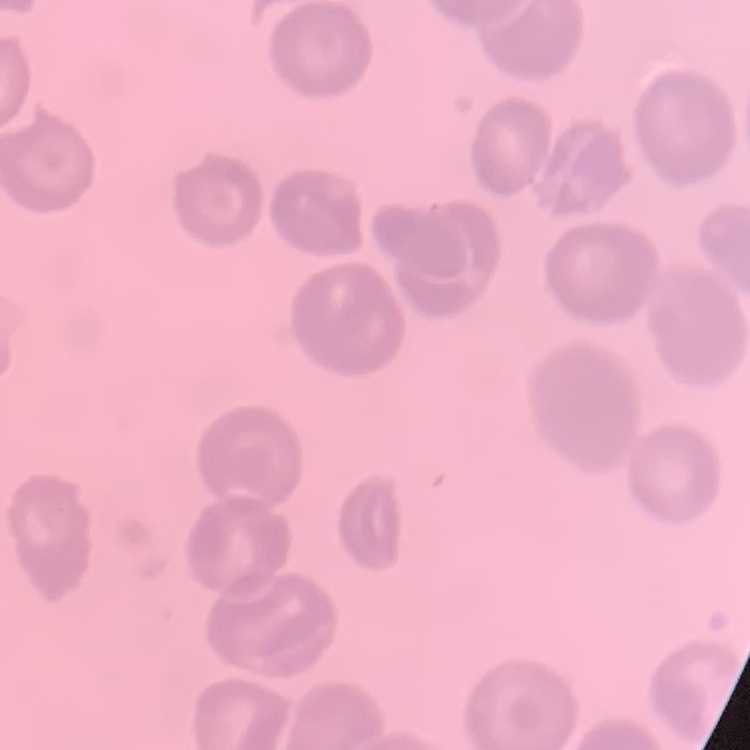

red blood cell morphology = no rouleaux formation
preparation = thin blood smear
image type = square crop of a larger photomicrograph
stain = Field's or Giemsa